Report the malaria status of this cell.
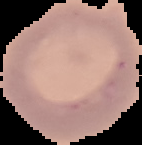

Uninfected.

Image is 142×145 pixels. From a thin blood smear. Cell region segmented out of the field of view; the surrounding area is masked to black.